Outline each blood parasite and name the species.
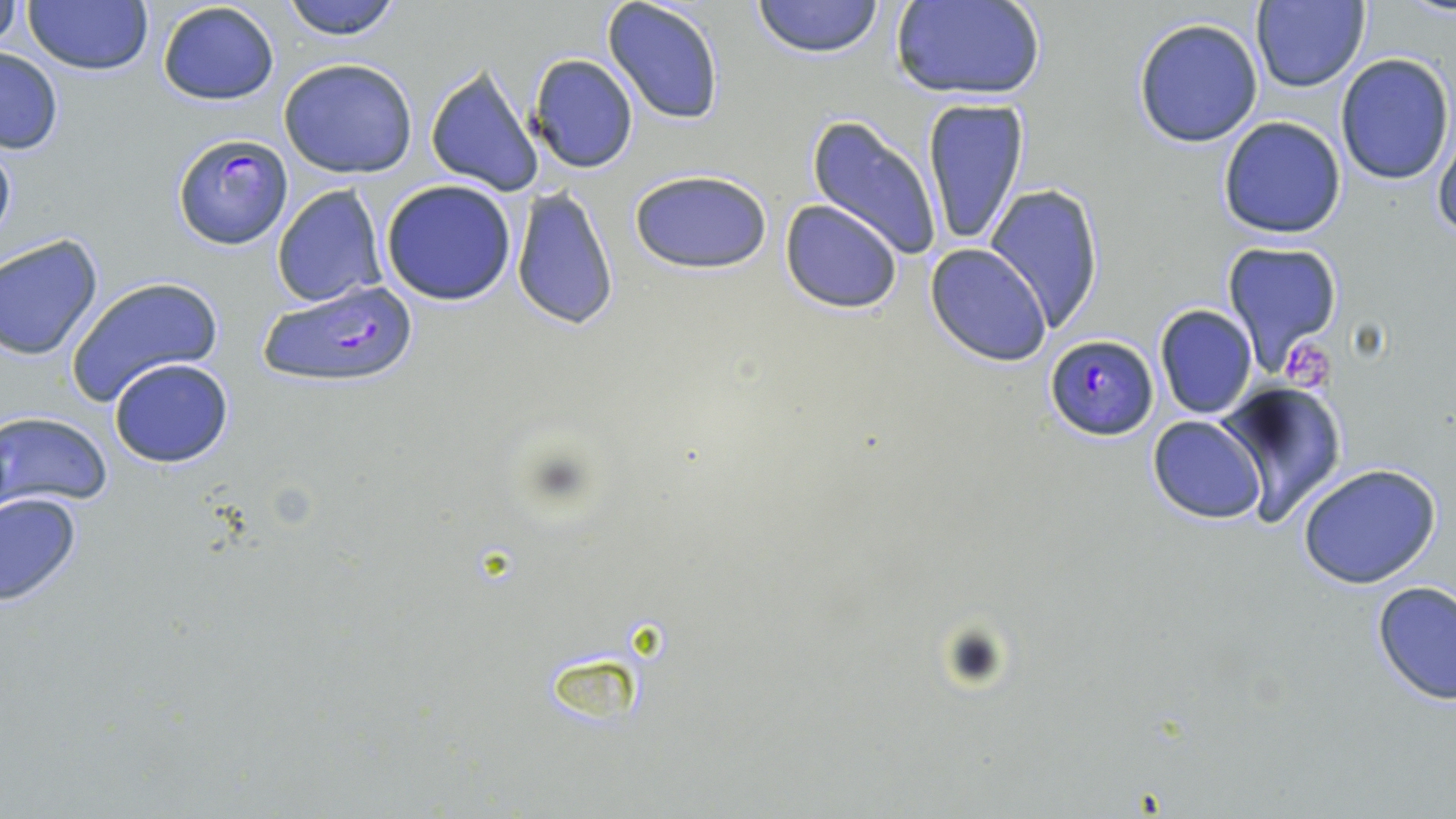

Approximate bounding boxes as (x1,y1)-(x2,y2) corner pairs in pixels.
Plasmodium falciparum-infected red blood cells: (170,132)-(294,251), (258,278)-(422,391), (1043,334)-(1158,441).
No Plasmodium ovale, Plasmodium malariae, Plasmodium vivax, Babesia divergens, or Trypanosoma brucei observed.

Summary:
  - Uninfected red blood cell locations: (280,0)-(403,41), (752,0)-(886,57), (1251,0)-(1370,92), (0,1)-(23,54), (23,1)-(154,77), (157,1)-(281,106), (601,1)-(724,125), (893,1)-(1044,100), (1132,16)-(1265,149), (0,46)-(64,157), (1334,53)-(1454,186), (529,54)-(640,174), (278,58)-(418,179), (425,65)-(543,198), (920,98)-(1030,249), (806,114)-(944,264), (1218,116)-(1347,239), (1432,118)-(1456,245), (0,130)-(17,256), (629,167)-(772,275), (381,179)-(518,305), (987,183)-(1105,331), (271,184)-(388,308), (510,187)-(618,331), (781,200)-(903,313), (0,236)-(104,360), (1222,241)-(1342,370), (925,243)-(1052,367), (64,275)-(226,409), (1154,304)-(1257,420), (108,357)-(234,469), (1222,382)-(1346,523), (1,411)-(113,510), (1149,416)-(1267,524), (1296,462)-(1444,589), (1,492)-(83,606), (1373,582)-(1456,704)
  - Platelet locations: (1284,342)-(1338,395)
  - Slide-level diagnosis: Plasmodium falciparum
  - Image size: 1456×819 pixels
  - Preparation: thin blood film
  - Magnification: 1000x
  - Field of view: one of a larger specimen
  - Stain: May-Grünwald-Giemsa
  - Modality: light microscopy